Classify this cell by malaria status.
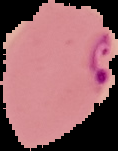
It is parasitized.

Image is 118×151 pixels. The area outside the segmented cell region is set to black. From a thin blood smear.